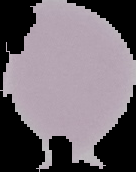

Summary:
  - Malaria status: uninfected
  - Preparation: thin blood film
  - Image size: 136×172 pixels
  - Image type: segmented cell region with the area outside set to black